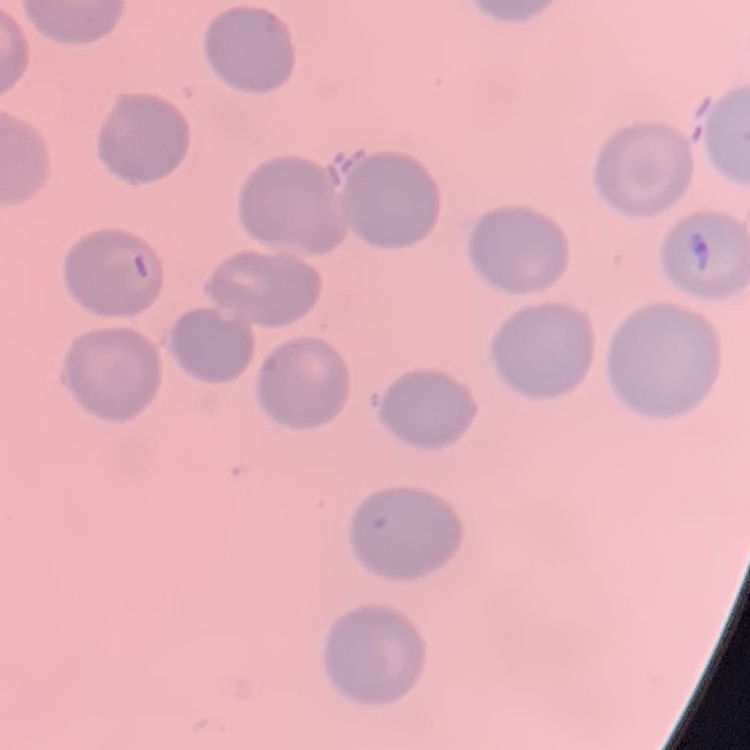

red blood cell morphology = no rouleaux formation
stain = Field's or Giemsa
preparation = thin blood film
image type = square crop of a larger photomicrograph